Report the malaria status of this cell.
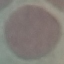

It is uninfected.

Summary:
  - Preparation: thin blood film
  - Capture: smartphone camera at the microscope eyepiece
  - Stain: Giemsa
  - Image type: cell patch, automatically extracted from a larger field of view and resized to 64 × 64 pixels